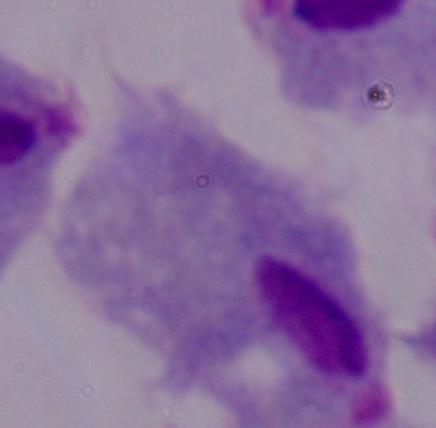

Summary:
  - Modality: photomicrograph
  - Identification: trichomonad
  - Magnification: 1000x